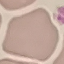
Malaria status: uninfected. Cell patch, automatically extracted from a larger field of view and resized to 64 × 64 pixels. Acquired by smartphone through the microscope eyepiece. Thin smear of blood. Giemsa-stained preparation.